Report the malaria status.
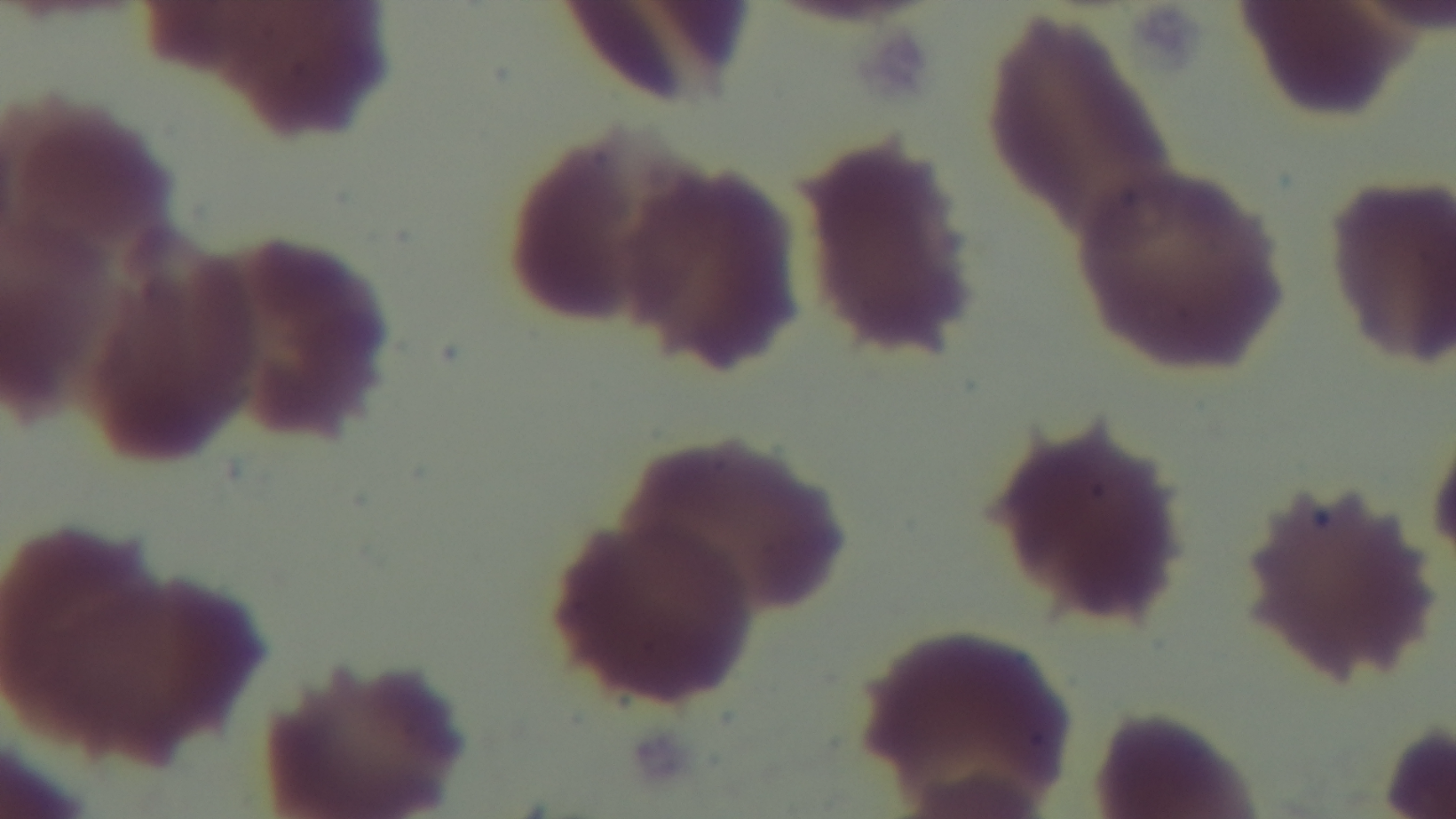

It is uninfected.

Photomicrograph. Mounted 4K digital camera. Giemsa-stained. Oil-immersion objective, 100x. One field from the slide. Preparation: thin smear.